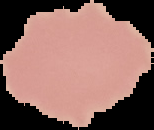

image size = 154×130 pixels
preparation = thin blood film
result = no malaria parasites seen
image type = segmented cell region with the area outside set to black